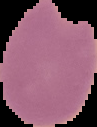
image type = segmented cell region with the area outside set to black
result = Plasmodium parasites identified
preparation = thin blood smear
image size = 97×127 pixels